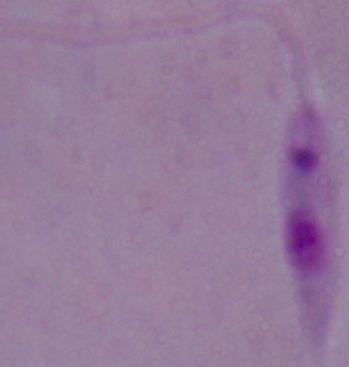
A Leishmania parasite is seen. Photomicrograph. Captured at 1000x magnification.